Assess this cell for malaria.
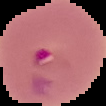

Parasitized.

image type = segmented cell region with the area outside set to black
image size = 106×106 pixels
preparation = thin blood smear